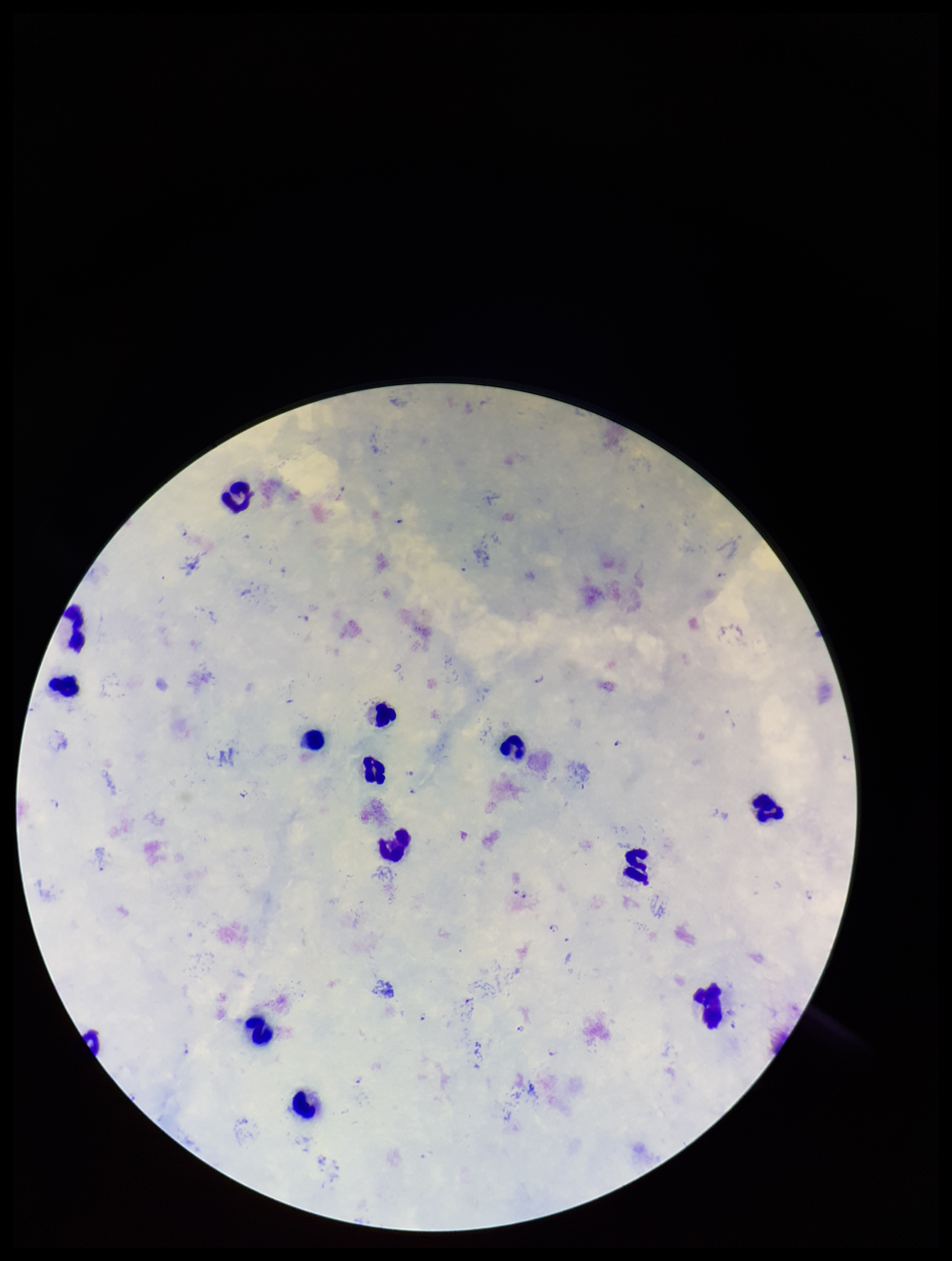

Plasmodium parasites = identified
image size = 952×1261 pixels
stain = Giemsa
capture = smartphone photograph through the microscope eyepiece
field of view = single
parasite count = 11
preparation = thick blood smear
patient malaria status = infected
species reported for this patient = Plasmodium falciparum
leukocyte count = 14